Name the parasite shown.
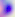

This is Toxoplasma gondii.

Captured at 400x magnification. Micrograph.